Classify this cell by malaria status.
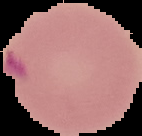
It is parasitized.

Summary:
  - Image type: cell region segmented out of the field of view; surrounding area masked to black
  - Image size: 142×136 pixels
  - Preparation: thin blood smear